Give the extent of all Babesia divergens-infected red blood cells.
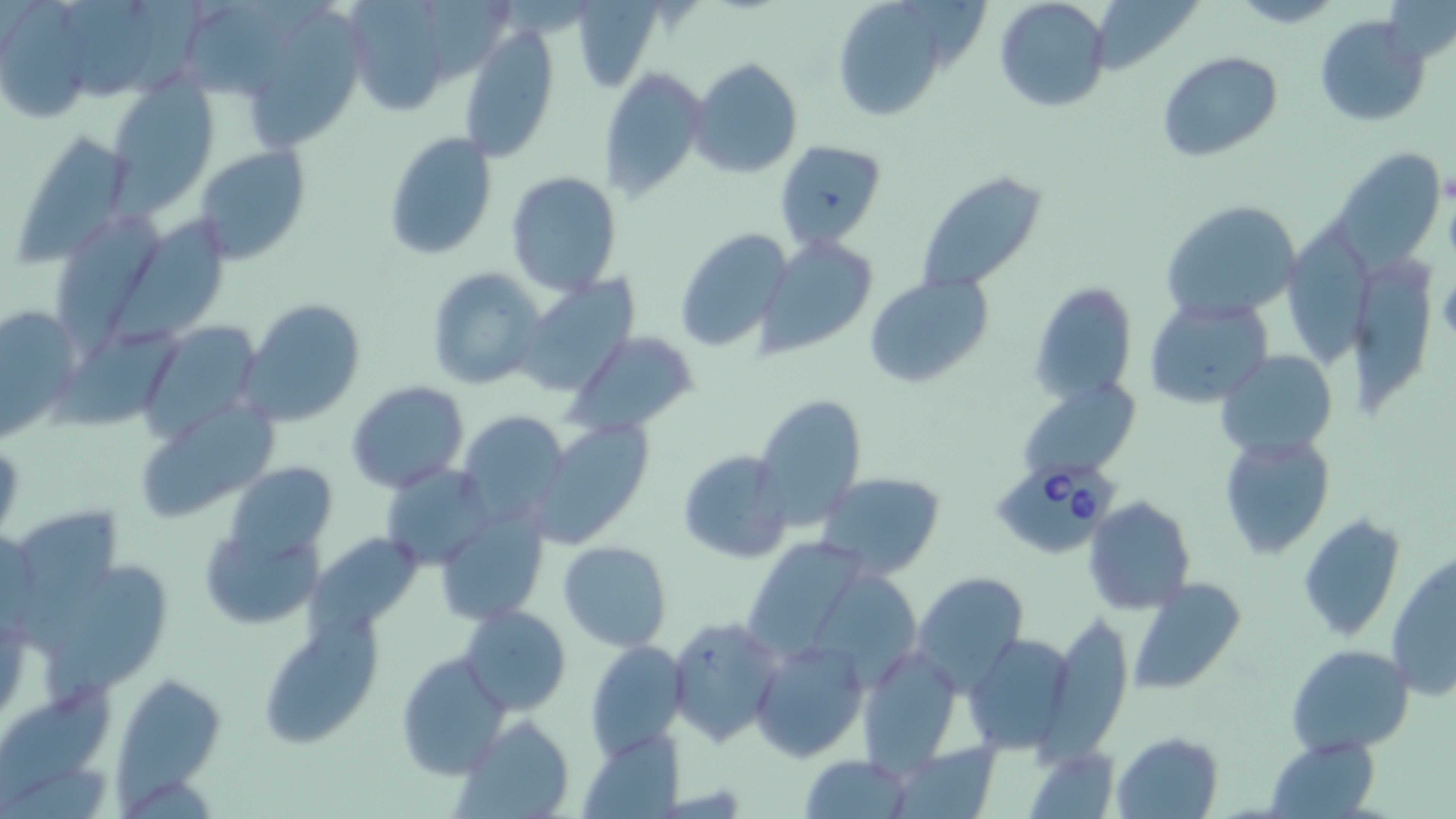

Approximate bounding boxes as named x1/y1/x2/y2 corners in pixels.
Babesia divergens-infected red blood cells: (x1=989, y1=457, x2=1121, y2=551).

{
  "slide_level_diagnosis": "Babesia divergens",
  "uninfected_red_blood_cell_locations": "approximate bounding boxes as named x1/y1/x2/y2 corners in pixels: (x1=355, y1=0, x2=452, y2=110), (x1=993, y1=0, x2=1111, y2=113), (x1=184, y1=1, x2=331, y2=95), (x1=829, y1=1, x2=951, y2=119), (x1=67, y1=2, x2=164, y2=94), (x1=3, y1=4, x2=94, y2=118), (x1=250, y1=9, x2=369, y2=149), (x1=1315, y1=14, x2=1430, y2=125), (x1=458, y1=24, x2=559, y2=162), (x1=1158, y1=51, x2=1283, y2=163), (x1=689, y1=57, x2=803, y2=177), (x1=596, y1=67, x2=705, y2=201), (x1=108, y1=80, x2=218, y2=207), (x1=382, y1=133, x2=496, y2=261), (x1=11, y1=134, x2=132, y2=263), (x1=774, y1=141, x2=886, y2=249), (x1=193, y1=145, x2=310, y2=264), (x1=1331, y1=146, x2=1447, y2=267), (x1=505, y1=172, x2=625, y2=296), (x1=915, y1=172, x2=1049, y2=294), (x1=1159, y1=199, x2=1300, y2=322), (x1=62, y1=201, x2=159, y2=355), (x1=108, y1=213, x2=242, y2=344), (x1=1280, y1=220, x2=1374, y2=371), (x1=673, y1=228, x2=794, y2=351), (x1=759, y1=237, x2=879, y2=356), (x1=1352, y1=254, x2=1435, y2=416), (x1=426, y1=266, x2=545, y2=389), (x1=865, y1=275, x2=991, y2=389), (x1=513, y1=278, x2=638, y2=399), (x1=1030, y1=284, x2=1137, y2=405), (x1=1145, y1=296, x2=1273, y2=406), (x1=238, y1=299, x2=365, y2=427), (x1=0, y1=305, x2=78, y2=436), (x1=142, y1=322, x2=263, y2=436), (x1=564, y1=329, x2=701, y2=437), (x1=54, y1=330, x2=184, y2=429), (x1=1218, y1=349, x2=1337, y2=458), (x1=346, y1=381, x2=468, y2=491), (x1=1023, y1=387, x2=1136, y2=476), (x1=754, y1=393, x2=868, y2=527), (x1=136, y1=400, x2=276, y2=522), (x1=458, y1=411, x2=569, y2=521), (x1=529, y1=420, x2=655, y2=548), (x1=1219, y1=431, x2=1336, y2=561), (x1=677, y1=448, x2=794, y2=563), (x1=224, y1=460, x2=337, y2=563), (x1=382, y1=463, x2=495, y2=569), (x1=815, y1=471, x2=947, y2=579), (x1=1084, y1=496, x2=1194, y2=614), (x1=437, y1=505, x2=549, y2=626), (x1=12, y1=507, x2=119, y2=657), (x1=1297, y1=512, x2=1407, y2=641), (x1=200, y1=525, x2=326, y2=630), (x1=309, y1=532, x2=421, y2=640), (x1=753, y1=535, x2=866, y2=650), (x1=557, y1=541, x2=672, y2=651), (x1=42, y1=553, x2=168, y2=707), (x1=1387, y1=555, x2=1456, y2=701), (x1=814, y1=563, x2=924, y2=684), (x1=910, y1=571, x2=1029, y2=695), (x1=1127, y1=578, x2=1248, y2=697), (x1=461, y1=605, x2=571, y2=715), (x1=664, y1=614, x2=783, y2=747), (x1=1045, y1=614, x2=1133, y2=754), (x1=256, y1=616, x2=380, y2=751), (x1=966, y1=633, x2=1076, y2=754), (x1=750, y1=638, x2=869, y2=762), (x1=584, y1=639, x2=688, y2=758), (x1=1285, y1=643, x2=1415, y2=756), (x1=858, y1=644, x2=961, y2=771), (x1=395, y1=651, x2=509, y2=778), (x1=119, y1=673, x2=227, y2=813), (x1=1, y1=682, x2=117, y2=814), (x1=456, y1=715, x2=576, y2=819), (x1=581, y1=730, x2=683, y2=817), (x1=1112, y1=732, x2=1223, y2=819), (x1=1264, y1=735, x2=1382, y2=819), (x1=889, y1=740, x2=1002, y2=817), (x1=801, y1=753, x2=916, y2=818)",
  "modality": "optical microscopy",
  "field_of_view": "single",
  "image_size": "1456×819 pixels",
  "magnification": "1000x",
  "preparation": "thin blood film",
  "stain": "May-Grünwald-Giemsa"
}